Classify this cell by malaria status.
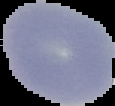

Uninfected.

Segmented cell region on a black background. Image is 115×106 pixels. From a thin blood film.